Report the malaria status of this cell.
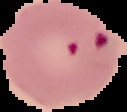

It is parasitized.

Image is 127×112 pixels. Segmented cell region on a black background. From a thin blood film.